Identify the preparation type.
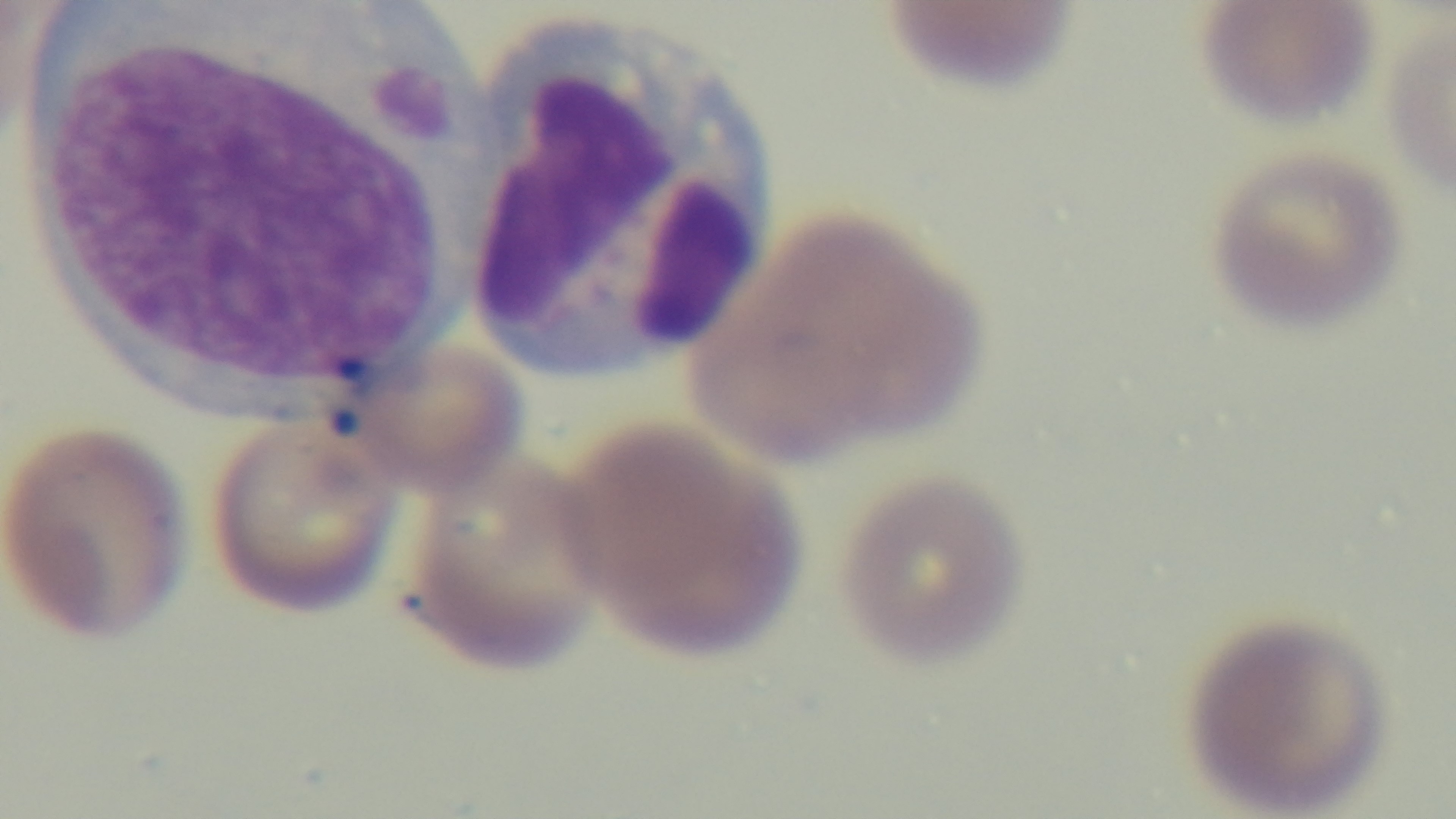

It is a thin blood film.

modality = light microscopy
field of view = single
malaria status = positive
capture = mounted 4K digital camera
stain = Giemsa
objective = 100x oil immersion